Locate every Plasmodium parasite and every leukocyte.
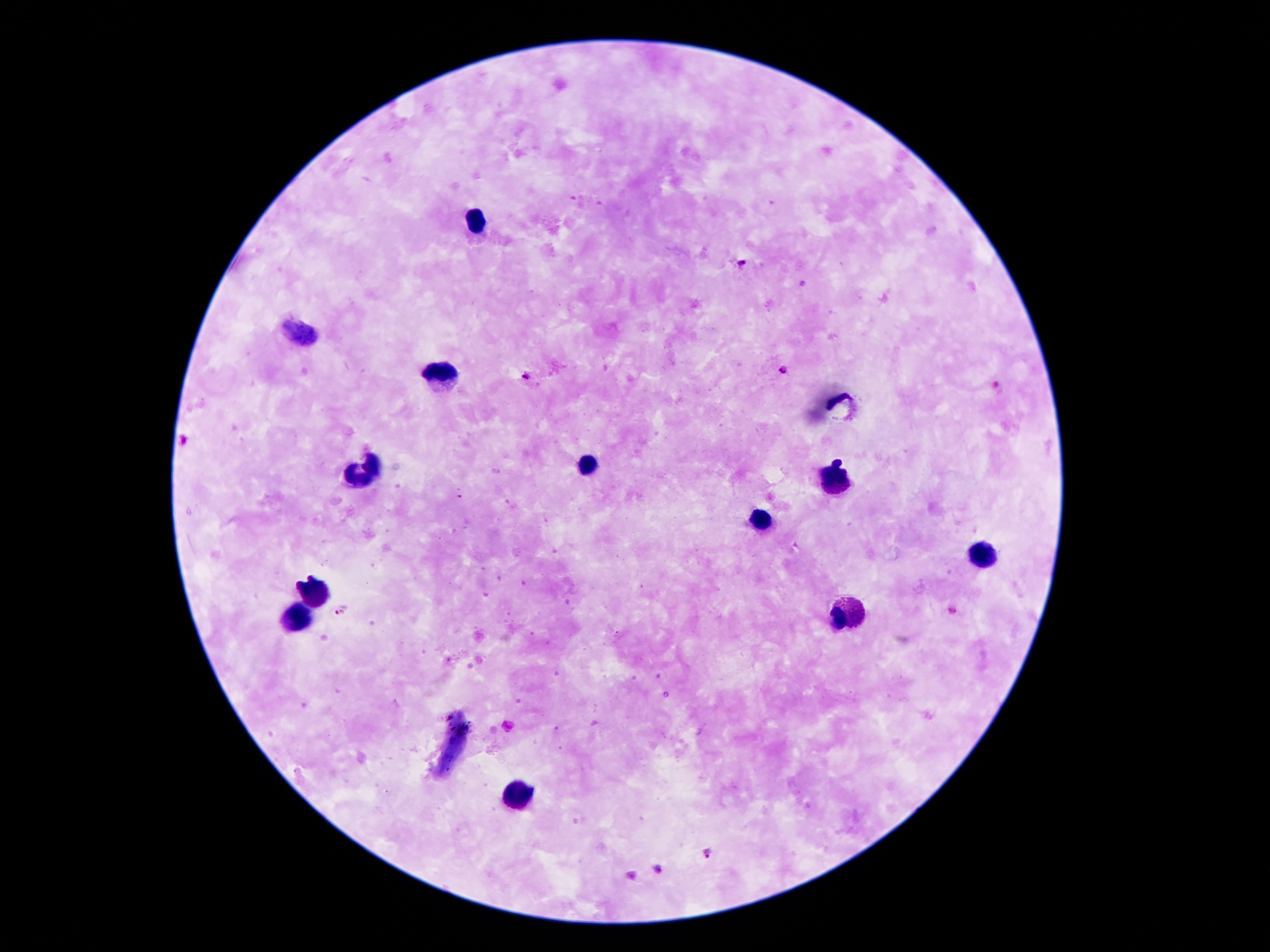
Approximate centers as (x, y) in pixels.
Plasmodium parasites: (740, 263), (784, 370), (527, 377), (339, 612), (709, 854), (659, 870), (631, 875).
Leukocytes: (478, 222), (442, 375), (584, 469), (368, 473), (832, 479), (758, 517), (981, 553), (312, 593), (850, 613), (298, 620), (522, 797).

patient_malaria_status: infected with Plasmodium falciparum
image_size: 1270×952 pixels
field_of_view: one from this slide
preparation: thick peripheral-blood smear
stain: Giemsa
magnification: 100x
capture: smartphone camera through the microscope eyepiece